Name the blood parasite species.
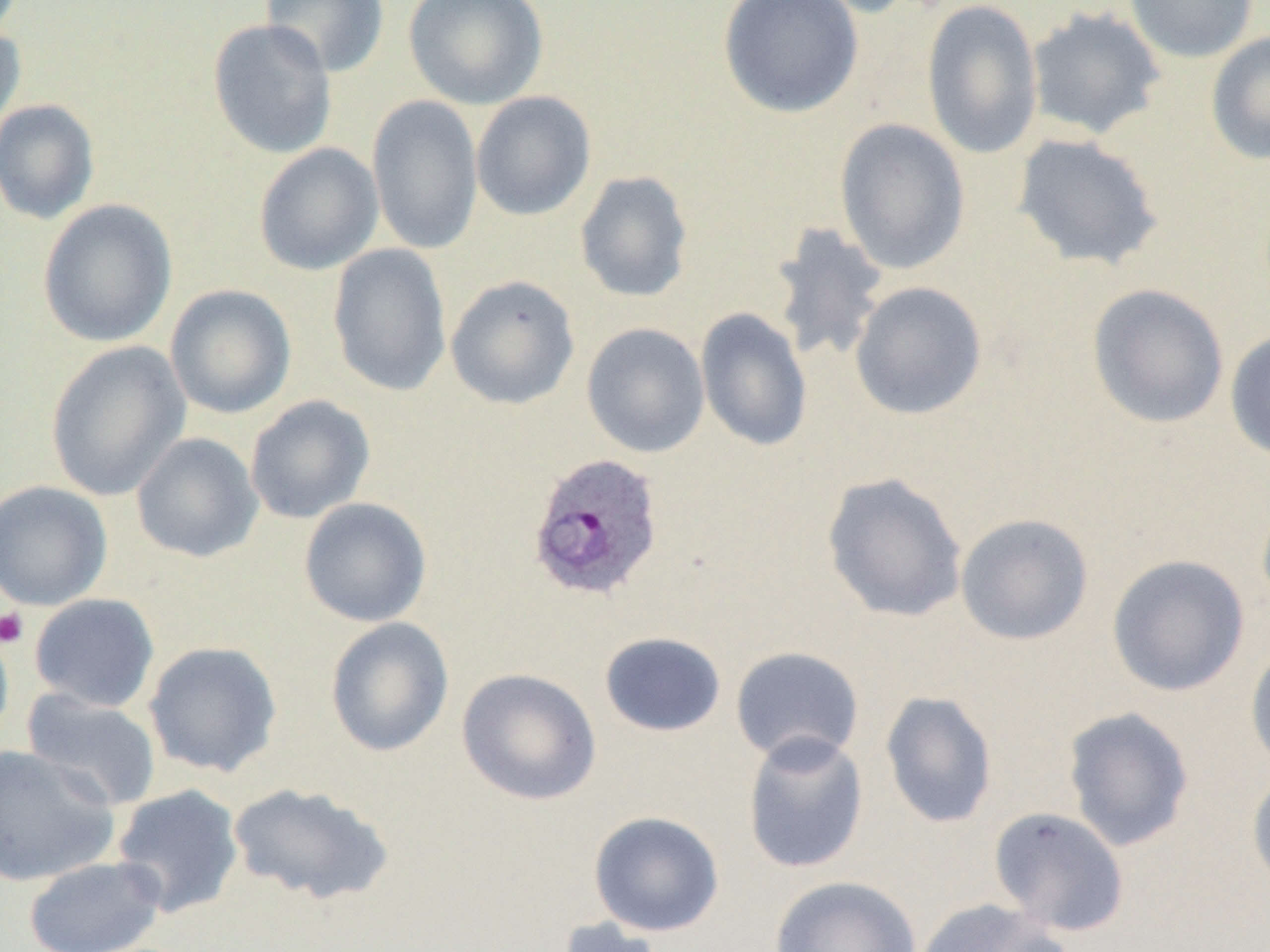

Plasmodium ovale.

Summary:
  - Coordinate format: approximate bounding boxes as (x1, y1, x2, y2) in pixels
  - Uninfected red blood cell locations: (261, 0, 390, 78), (403, 0, 548, 109), (718, 0, 864, 119), (789, 0, 919, 19), (921, 0, 1044, 160), (1124, 0, 1259, 63), (1025, 6, 1167, 140), (207, 18, 338, 160), (0, 20, 27, 140), (1205, 31, 1270, 166), (470, 90, 597, 221), (367, 94, 484, 256), (0, 99, 100, 224), (833, 118, 971, 275), (1011, 133, 1164, 272), (253, 143, 384, 276), (574, 170, 694, 303), (37, 199, 178, 348), (767, 221, 890, 366), (328, 243, 452, 398), (445, 275, 580, 410), (849, 281, 988, 421), (1087, 283, 1230, 429), (165, 284, 296, 419), (695, 307, 813, 453), (581, 322, 710, 458), (1225, 328, 1270, 464), (44, 340, 191, 501), (245, 395, 376, 524), (131, 432, 264, 563), (821, 472, 968, 623), (0, 480, 113, 611), (298, 496, 433, 628), (955, 512, 1094, 645), (1106, 554, 1250, 697), (29, 593, 160, 713), (325, 616, 455, 757), (0, 620, 14, 750), (598, 631, 726, 737), (1245, 639, 1270, 776), (143, 641, 283, 777), (730, 646, 865, 766), (456, 667, 602, 806), (21, 687, 163, 813), (880, 690, 998, 829), (1063, 706, 1195, 852), (741, 730, 870, 875), (0, 745, 120, 886), (1247, 768, 1270, 893), (228, 781, 394, 906), (111, 784, 244, 918), (988, 806, 1131, 937), (588, 811, 724, 937), (23, 856, 166, 952), (769, 875, 922, 952), (914, 897, 1070, 952), (555, 917, 669, 952)
  - Plasmodium ovale-infected red blood cell locations: (527, 452, 665, 602)
  - Platelet locations: (0, 608, 29, 648)
  - Preparation: thin blood smear
  - Image size: 1270×952 pixels
  - Magnification: 1000x
  - Field of view: single
  - Modality: light microscopy